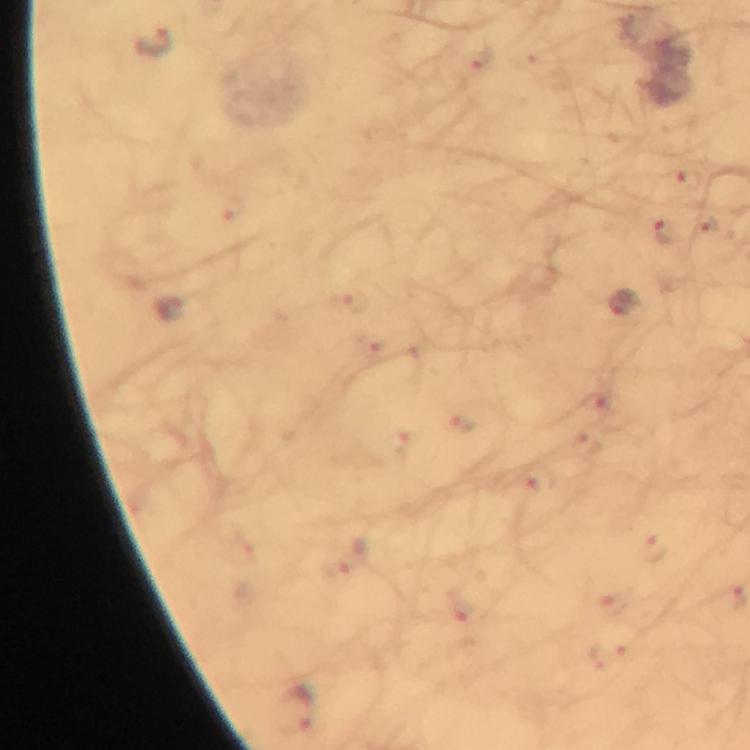
stain: Giemsa
cropped_from: one field of view
magnification: 100x
immersion_oil: used
preparation: thick blood film
capture: smartphone mounted on the microscope
plasmodium_parasite_locations: 'approximate centers as (x, y) in pixels: (154, 41), (665, 230), (622, 302)'
image_size: 750×750 pixels
context: from a malaria diagnostic workup